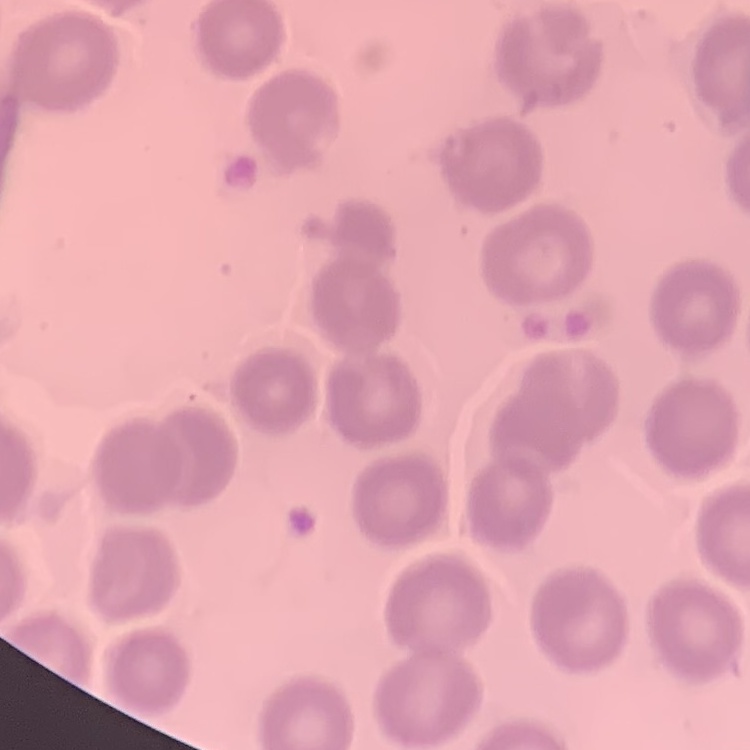
Summary:
  - Red blood cell morphology: no rouleaux formation
  - Stain: Field's or Giemsa
  - Image type: square crop of a larger photomicrograph
  - Preparation: thin blood film